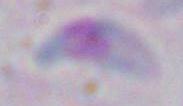
Micrograph. Toxoplasma gondii is seen. 1000x magnification.